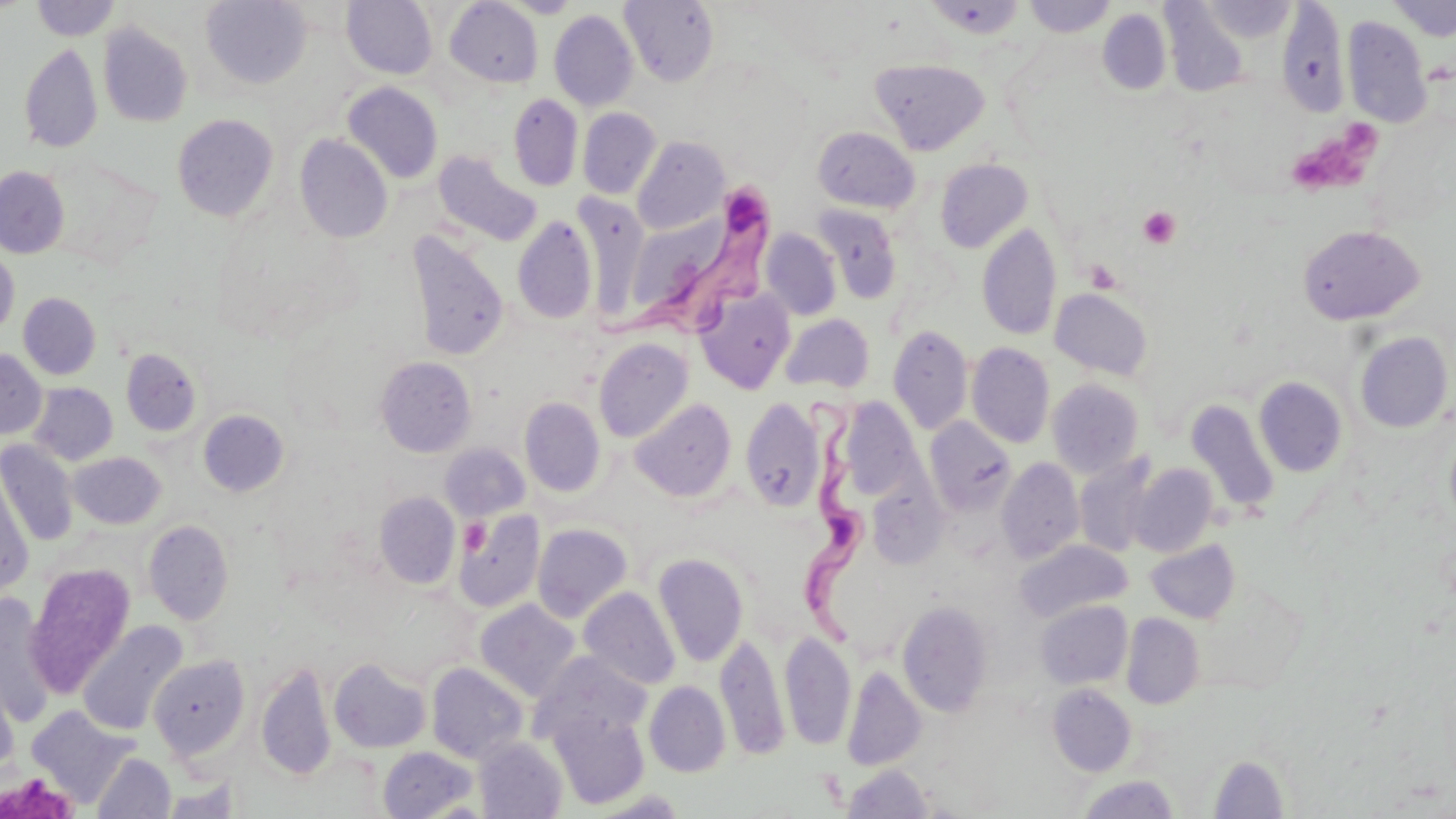

slide_level_diagnosis: Trypanosoma brucei
image_size: 1456×819 pixels
magnification: 1000x
modality: light microscopy
trypanosoma_brucei_locations: 'approximate bounding boxes as named x1/y1/x2/y2 corners in pixels: (x1=587, y1=170, x2=784, y2=337), (x1=798, y1=395, x2=866, y2=663)'
uninfected_red_blood_cell_locations: 'approximate bounding boxes as named x1/y1/x2/y2 corners in pixels: (x1=30, y1=0, x2=121, y2=41), (x1=341, y1=0, x2=437, y2=78), (x1=504, y1=0, x2=581, y2=18), (x1=619, y1=0, x2=719, y2=87), (x1=923, y1=0, x2=1027, y2=40), (x1=1023, y1=0, x2=1115, y2=37), (x1=1390, y1=0, x2=1456, y2=40), (x1=200, y1=1, x2=311, y2=89), (x1=443, y1=1, x2=543, y2=88), (x1=1202, y1=1, x2=1296, y2=41), (x1=1277, y1=3, x2=1350, y2=117), (x1=1162, y1=4, x2=1249, y2=97), (x1=1098, y1=8, x2=1171, y2=96), (x1=549, y1=10, x2=638, y2=111), (x1=1342, y1=15, x2=1432, y2=127), (x1=98, y1=23, x2=193, y2=127), (x1=19, y1=43, x2=102, y2=154), (x1=871, y1=58, x2=989, y2=154), (x1=342, y1=82, x2=443, y2=184), (x1=508, y1=93, x2=583, y2=191), (x1=578, y1=108, x2=661, y2=198), (x1=172, y1=114, x2=278, y2=221), (x1=813, y1=127, x2=919, y2=213), (x1=294, y1=134, x2=393, y2=243), (x1=632, y1=137, x2=728, y2=234), (x1=433, y1=149, x2=542, y2=246), (x1=935, y1=158, x2=1033, y2=253), (x1=0, y1=167, x2=69, y2=258), (x1=573, y1=193, x2=652, y2=319), (x1=626, y1=200, x2=773, y2=332), (x1=812, y1=205, x2=902, y2=304), (x1=512, y1=217, x2=598, y2=324), (x1=977, y1=223, x2=1061, y2=341), (x1=1297, y1=225, x2=1425, y2=325), (x1=760, y1=229, x2=842, y2=320), (x1=405, y1=231, x2=509, y2=361), (x1=0, y1=247, x2=19, y2=339), (x1=1050, y1=288, x2=1154, y2=381), (x1=695, y1=290, x2=795, y2=393), (x1=18, y1=292, x2=101, y2=379), (x1=781, y1=313, x2=875, y2=394), (x1=888, y1=325, x2=972, y2=435), (x1=1354, y1=331, x2=1453, y2=433), (x1=593, y1=337, x2=693, y2=443), (x1=967, y1=343, x2=1054, y2=448), (x1=120, y1=348, x2=202, y2=437), (x1=0, y1=349, x2=46, y2=439), (x1=375, y1=356, x2=476, y2=457), (x1=1254, y1=377, x2=1348, y2=478), (x1=1047, y1=378, x2=1144, y2=479), (x1=30, y1=383, x2=118, y2=465), (x1=520, y1=397, x2=605, y2=496), (x1=740, y1=397, x2=825, y2=512), (x1=837, y1=397, x2=921, y2=499), (x1=630, y1=398, x2=737, y2=502), (x1=1186, y1=399, x2=1281, y2=516), (x1=198, y1=410, x2=289, y2=497), (x1=924, y1=417, x2=1017, y2=516), (x1=1445, y1=423, x2=1456, y2=532), (x1=0, y1=440, x2=78, y2=546), (x1=440, y1=443, x2=529, y2=520), (x1=68, y1=451, x2=166, y2=529), (x1=1074, y1=454, x2=1159, y2=557), (x1=996, y1=458, x2=1084, y2=564), (x1=1127, y1=463, x2=1218, y2=557), (x1=1, y1=471, x2=35, y2=595), (x1=867, y1=477, x2=949, y2=569), (x1=374, y1=492, x2=460, y2=589), (x1=453, y1=509, x2=545, y2=614), (x1=143, y1=520, x2=234, y2=625), (x1=532, y1=524, x2=633, y2=622), (x1=1145, y1=539, x2=1240, y2=623), (x1=1015, y1=540, x2=1132, y2=622), (x1=653, y1=552, x2=749, y2=667), (x1=25, y1=563, x2=136, y2=698), (x1=579, y1=587, x2=680, y2=690), (x1=0, y1=594, x2=57, y2=725), (x1=475, y1=600, x2=580, y2=702), (x1=897, y1=600, x2=994, y2=716), (x1=1036, y1=601, x2=1132, y2=689), (x1=1121, y1=613, x2=1204, y2=709), (x1=78, y1=620, x2=187, y2=737), (x1=715, y1=630, x2=789, y2=762), (x1=779, y1=630, x2=856, y2=751), (x1=531, y1=652, x2=651, y2=751), (x1=147, y1=655, x2=250, y2=762), (x1=329, y1=657, x2=432, y2=753), (x1=256, y1=661, x2=337, y2=780), (x1=426, y1=662, x2=529, y2=764), (x1=842, y1=665, x2=926, y2=772), (x1=0, y1=672, x2=19, y2=780), (x1=644, y1=681, x2=731, y2=776), (x1=1047, y1=684, x2=1137, y2=776), (x1=26, y1=706, x2=138, y2=809), (x1=548, y1=709, x2=650, y2=810), (x1=474, y1=737, x2=568, y2=819), (x1=378, y1=746, x2=478, y2=818), (x1=92, y1=752, x2=176, y2=818), (x1=1208, y1=754, x2=1289, y2=818), (x1=841, y1=764, x2=935, y2=818), (x1=1078, y1=775, x2=1179, y2=818), (x1=157, y1=781, x2=243, y2=818)'
field_of_view: single
preparation: thin blood film
platelet_locations: 'approximate bounding boxes as named x1/y1/x2/y2 corners in pixels: (x1=1299, y1=131, x2=1388, y2=187), (x1=1138, y1=206, x2=1181, y2=249)'
stain: May-Grünwald-Giemsa